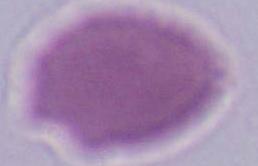
Summary:
  - Magnification: 1000x
  - Identification: red blood cell
  - Modality: photomicrograph